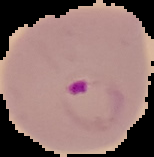

From a thin blood smear. Segmented cell region on a black background. Image is 154×157 pixels. Malaria status: parasitized.